Name the parasite shown.
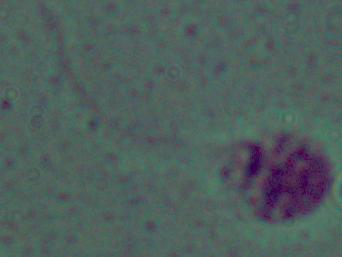

Leishmania.

Summary:
  - Modality: micrograph
  - Magnification: 1000x